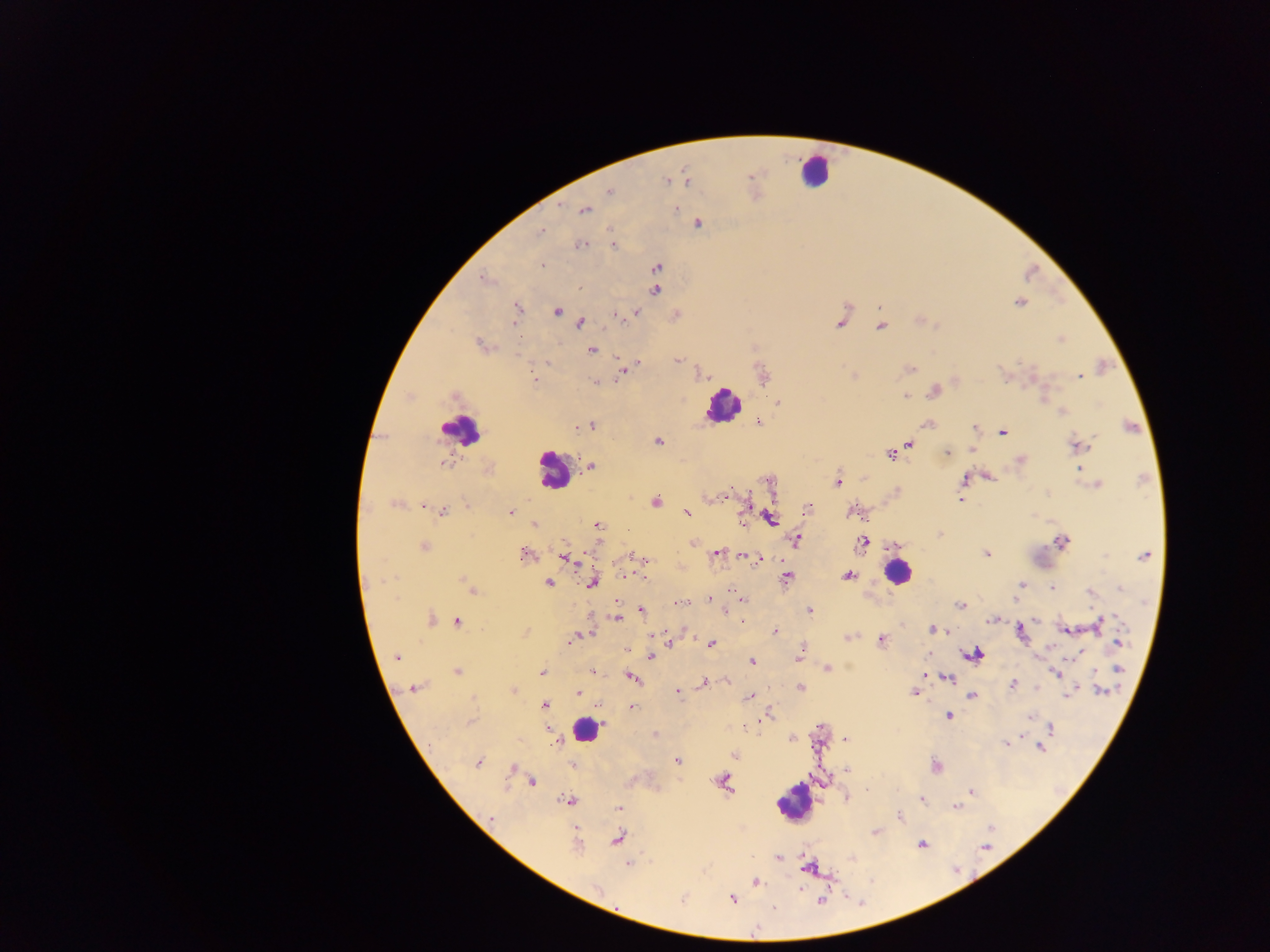

Approximate centers as [x, y] in pixels.
Summary:
  - Leukocyte locations: [814, 171], [723, 407], [459, 429], [553, 470], [897, 572], [585, 730], [792, 802]
  - Malaria parasite locations: [750, 177], [685, 180], [666, 181], [610, 191], [676, 209], [584, 210], [698, 223], [541, 231], [581, 245], [613, 245], [541, 265], [657, 267], [484, 278], [578, 288], [656, 289], [1019, 302], [518, 308], [557, 311], [636, 312], [617, 316], [624, 318], [580, 323], [513, 324], [839, 324], [881, 327], [1061, 340], [480, 344], [592, 350], [678, 359], [547, 363], [638, 363], [909, 369], [624, 371], [704, 375], [1079, 376], [534, 379], [596, 381], [934, 391], [905, 396], [454, 397], [778, 403], [1062, 412], [759, 422], [928, 424], [591, 425], [976, 428], [1003, 432], [658, 441], [910, 444], [1079, 446], [972, 450], [947, 453], [890, 455], [1020, 460], [444, 464], [591, 467], [1079, 470], [988, 477], [964, 479], [838, 481], [1097, 484], [656, 500], [960, 500], [396, 504], [746, 504], [423, 507], [808, 508], [443, 510], [687, 512], [512, 513], [853, 513], [771, 518], [534, 524], [598, 525], [795, 540], [862, 542], [1061, 542], [693, 544], [424, 546], [717, 553], [525, 554], [986, 554], [633, 556], [1105, 556], [1144, 556], [639, 557], [566, 558], [752, 559], [627, 575], [848, 575], [644, 577], [787, 578], [464, 580], [548, 583], [593, 583], [1020, 584], [1052, 588], [1120, 588], [472, 590], [1091, 593], [710, 599], [742, 600], [679, 603], [959, 604], [642, 610], [810, 610], [726, 612], [622, 615], [616, 617], [431, 619], [992, 619], [742, 621], [458, 622], [1102, 623], [934, 630], [1067, 630], [776, 632], [1021, 632], [588, 633], [580, 635], [848, 637], [572, 640], [881, 641], [669, 642], [1118, 642], [712, 643], [975, 654], [650, 656], [1073, 657], [396, 658], [798, 659], [751, 662], [828, 668], [1118, 669], [457, 671], [592, 671], [541, 672], [1056, 673], [923, 674], [632, 677], [946, 677], [704, 682], [1012, 685], [800, 687], [413, 688], [513, 690], [1102, 690], [676, 692], [578, 693], [913, 693], [1070, 694], [750, 696], [971, 696], [545, 706], [632, 706], [769, 713], [948, 716], [1029, 717], [469, 722], [1051, 728], [655, 734], [793, 738], [846, 739], [554, 741], [1006, 743], [1040, 747], [734, 755], [677, 761], [477, 762], [572, 765], [935, 766], [513, 768], [846, 769], [723, 781], [532, 782], [971, 791], [568, 800], [922, 800], [618, 808], [956, 808], [492, 817], [899, 817], [875, 832], [618, 839], [922, 844], [576, 845], [985, 848], [778, 858], [628, 864], [810, 867], [756, 882], [598, 889], [732, 899], [682, 900], [821, 901]
  - Capture: mobile-phone photograph through a microscope
  - Image size: 1270×952 pixels
  - Preparation: thick blood smear
  - Field of view: single
  - Country: Ghana